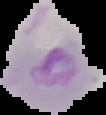
Summary:
  - Result: malaria parasites detected
  - Image size: 106×115 pixels
  - Preparation: thin blood film
  - Image type: segmented cell region on a black background